Assess this cell for malaria.
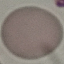

It is uninfected.

Cell patch, automatically extracted from a larger field of view and resized to 64 × 64 pixels. Thin blood film. Giemsa-stained preparation. Acquired by smartphone through the microscope eyepiece.